Look for Plasmodium parasites.
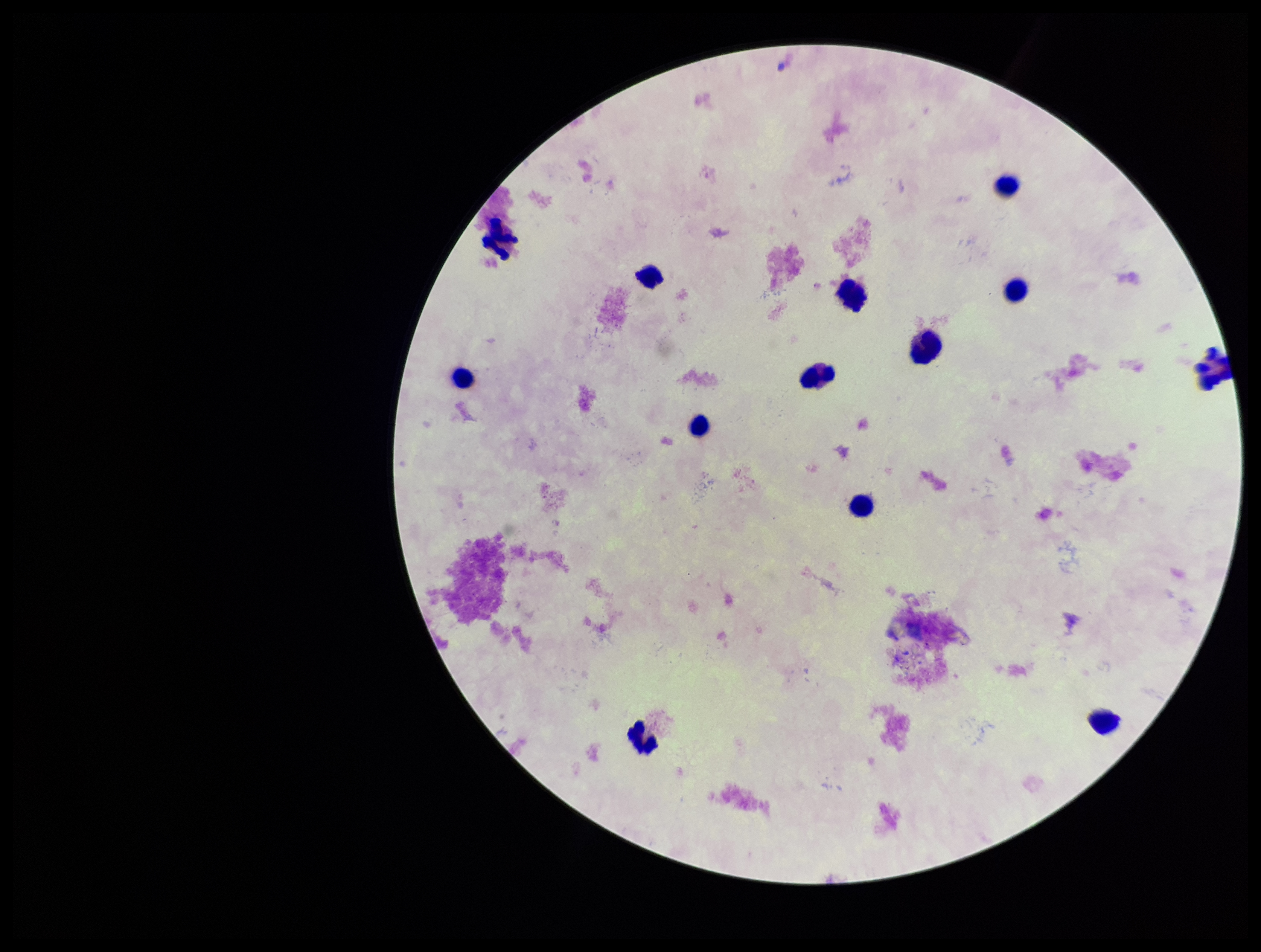

None detected.

patient malaria status = negative
preparation = thick
leukocyte count = 13
capture = smartphone photograph through the microscope eyepiece
parasite count = 0
image size = 1261×952 pixels
stain = Giemsa
field of view = one from this slide